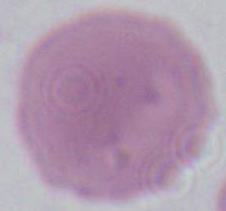

Summary:
  - Modality: photomicrograph
  - Magnification: 1000x
  - Identification: erythrocyte